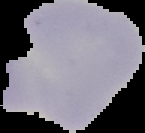
Summary:
  - Image size: 145×133 pixels
  - Result: no malaria parasites detected
  - Preparation: thin blood smear
  - Image type: segmented cell region with the area outside set to black